Report the malaria status of this cell.
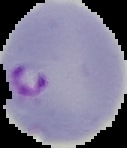
Parasitized.

The area outside the segmented cell region is set to black. Image is 127×148 pixels. From a thin blood film.